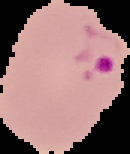

From a thin blood smear. Malaria status: parasitized. Image is 130×154 pixels. Cell region segmented out of the field of view; the surrounding area is masked to black.